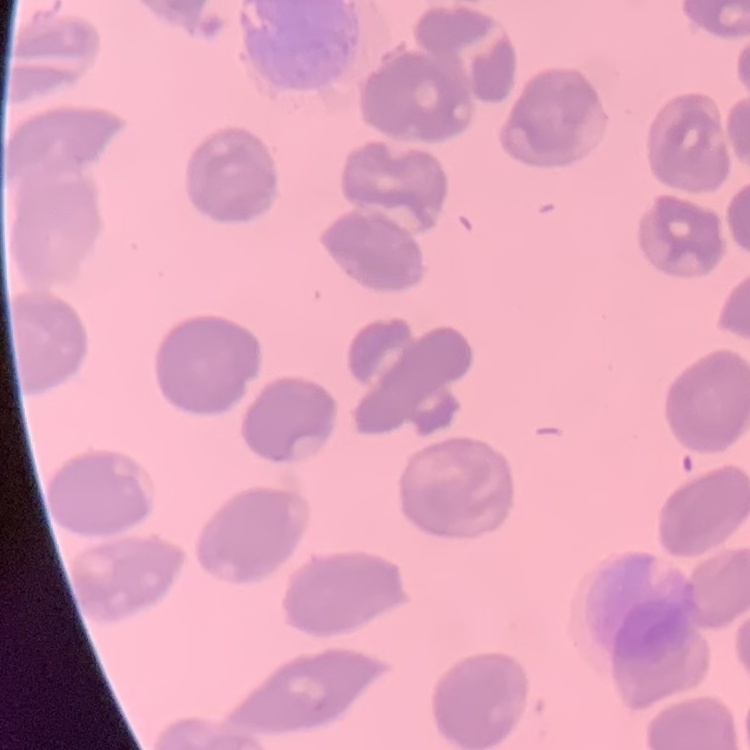

Summary:
  - Erythrocyte morphology: no rouleaux formation
  - Preparation: thin blood film
  - Stain: Field's or Giemsa
  - Image type: one tile cut from a larger photomicrograph